Outline each blood parasite and name the species.
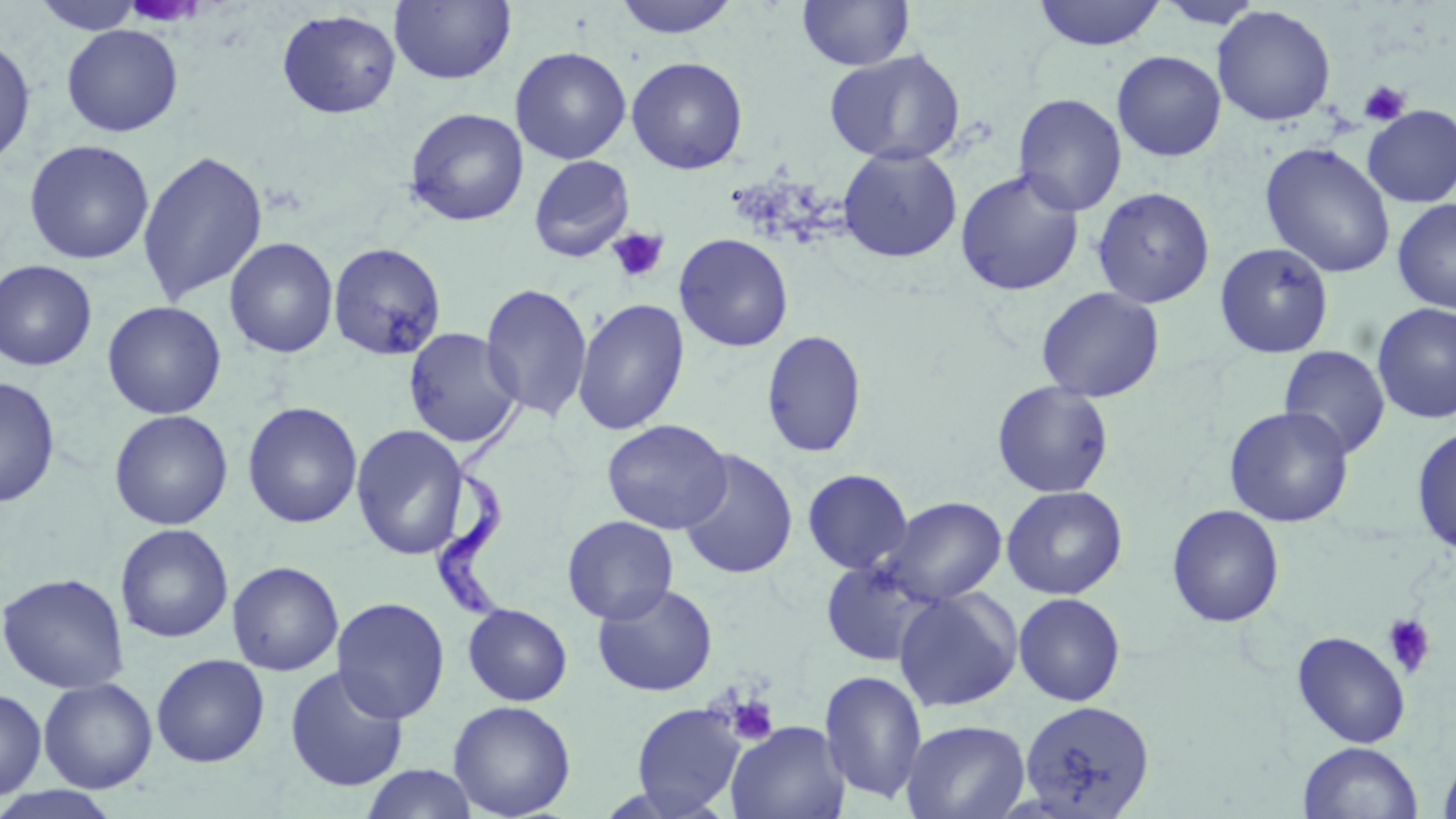

Approximate bounding boxes as named x1/y1/x2/y2 corners in pixels.
Trypanosoma brucei: (x1=433, y1=386, x2=534, y2=624).
No Plasmodium falciparum, Plasmodium ovale, Plasmodium malariae, Plasmodium vivax, or Babesia divergens observed.

Uninfected red blood cell locations: (x1=30, y1=0, x2=146, y2=34), (x1=389, y1=0, x2=516, y2=85), (x1=611, y1=0, x2=742, y2=39), (x1=797, y1=0, x2=914, y2=71), (x1=1032, y1=0, x2=1166, y2=50), (x1=1155, y1=1, x2=1265, y2=29), (x1=1211, y1=5, x2=1336, y2=126), (x1=276, y1=9, x2=402, y2=119), (x1=61, y1=24, x2=184, y2=137), (x1=0, y1=37, x2=36, y2=167), (x1=510, y1=46, x2=632, y2=164), (x1=824, y1=49, x2=966, y2=166), (x1=1112, y1=51, x2=1226, y2=161), (x1=626, y1=57, x2=748, y2=175), (x1=1013, y1=93, x2=1127, y2=216), (x1=1362, y1=105, x2=1456, y2=207), (x1=404, y1=108, x2=529, y2=226), (x1=23, y1=139, x2=155, y2=265), (x1=1260, y1=142, x2=1396, y2=278), (x1=837, y1=147, x2=962, y2=263), (x1=137, y1=150, x2=268, y2=305), (x1=528, y1=155, x2=635, y2=262), (x1=955, y1=169, x2=1085, y2=297), (x1=1091, y1=187, x2=1215, y2=309), (x1=1393, y1=199, x2=1456, y2=314), (x1=674, y1=233, x2=794, y2=352), (x1=224, y1=237, x2=339, y2=359), (x1=328, y1=242, x2=447, y2=361), (x1=1214, y1=243, x2=1334, y2=359), (x1=0, y1=260, x2=97, y2=371), (x1=480, y1=283, x2=594, y2=421), (x1=1036, y1=286, x2=1165, y2=403), (x1=573, y1=299, x2=690, y2=435), (x1=102, y1=300, x2=227, y2=419), (x1=1372, y1=302, x2=1456, y2=425), (x1=403, y1=327, x2=523, y2=448), (x1=761, y1=330, x2=867, y2=458), (x1=1278, y1=346, x2=1390, y2=459), (x1=0, y1=377, x2=60, y2=508), (x1=992, y1=380, x2=1114, y2=498), (x1=242, y1=401, x2=363, y2=529), (x1=1224, y1=406, x2=1354, y2=527), (x1=108, y1=409, x2=233, y2=530), (x1=602, y1=419, x2=732, y2=535), (x1=351, y1=424, x2=469, y2=560), (x1=1411, y1=426, x2=1456, y2=558), (x1=678, y1=449, x2=798, y2=580), (x1=803, y1=468, x2=913, y2=574), (x1=1001, y1=485, x2=1128, y2=600), (x1=881, y1=496, x2=1007, y2=605), (x1=1167, y1=505, x2=1285, y2=628), (x1=562, y1=515, x2=678, y2=624), (x1=115, y1=523, x2=233, y2=643), (x1=820, y1=558, x2=941, y2=666), (x1=227, y1=560, x2=343, y2=676), (x1=0, y1=572, x2=129, y2=694), (x1=591, y1=582, x2=718, y2=697), (x1=893, y1=588, x2=1022, y2=712), (x1=1013, y1=592, x2=1126, y2=707), (x1=331, y1=596, x2=451, y2=724), (x1=462, y1=603, x2=573, y2=706), (x1=1291, y1=630, x2=1411, y2=748), (x1=151, y1=653, x2=270, y2=767), (x1=284, y1=665, x2=409, y2=792), (x1=820, y1=668, x2=928, y2=805), (x1=37, y1=677, x2=158, y2=794), (x1=0, y1=687, x2=47, y2=800), (x1=447, y1=700, x2=576, y2=819), (x1=1020, y1=700, x2=1155, y2=818), (x1=630, y1=702, x2=745, y2=816), (x1=901, y1=719, x2=1030, y2=819), (x1=727, y1=721, x2=850, y2=819), (x1=1298, y1=741, x2=1424, y2=819), (x1=1437, y1=753, x2=1456, y2=819), (x1=359, y1=764, x2=480, y2=819), (x1=0, y1=786, x2=123, y2=819). Platelet locations: (x1=1358, y1=80, x2=1411, y2=126), (x1=608, y1=227, x2=670, y2=284), (x1=1382, y1=613, x2=1438, y2=679), (x1=726, y1=695, x2=779, y2=745). Slide-level diagnosis: Trypanosoma brucei. One field of a larger specimen. 1000x magnification. Thin blood smear. Light microscopy. May-Grünwald-Giemsa stain. Image is 1456×819 pixels.